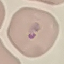 Malaria status: parasitized. Photographed with a smartphone camera at the microscope eyepiece. Automatically extracted cell patch, resized to 64 × 64 pixels. Thin blood smear. Giemsa-stained preparation.